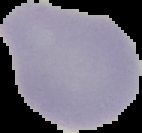
From a thin blood smear. Result: no malaria parasites detected. The area outside the segmented cell region is set to black. Image is 142×133 pixels.